State which parasite is depicted.
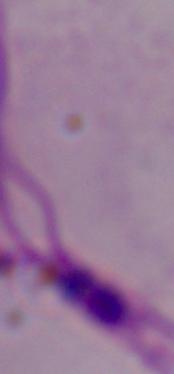
Leishmania.

Summary:
  - Magnification: 1000x
  - Modality: photomicrograph